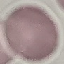 Malaria status: uninfected. Giemsa stain. Acquired by smartphone through the microscope eyepiece. Thin smear of blood. Automatically extracted cell patch, resized to 64 × 64 pixels.